State the preparation type.
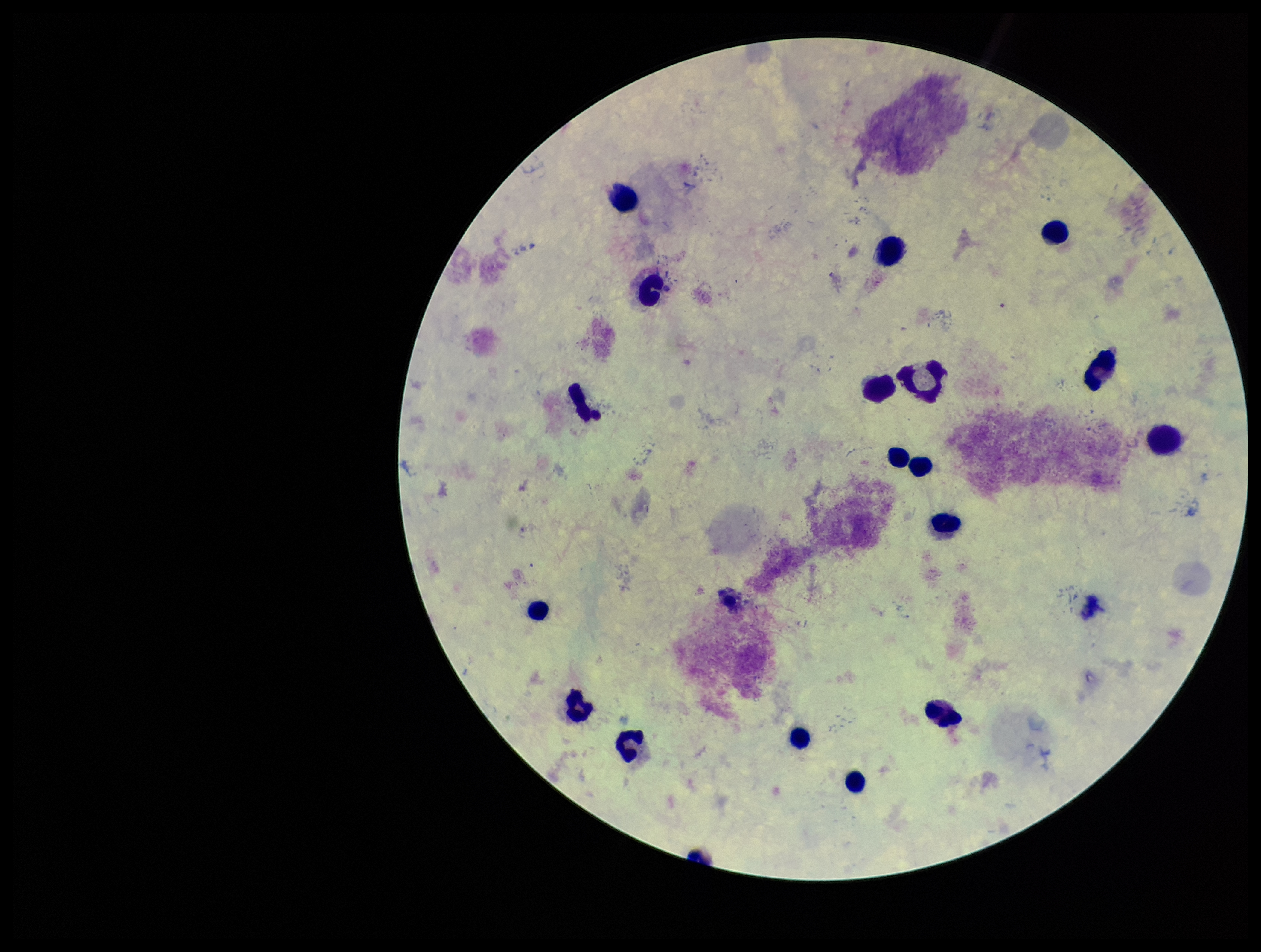

It is a thick blood smear.

Leukocyte count: 17. Photographed through the microscope eyepiece with a smartphone camera. Giemsa stain. Patient malaria status: negative. Image is 1261×952 pixels. Plasmodium parasites: none detected. Single field of view. Parasite count: 0.